Identify the preparation type.
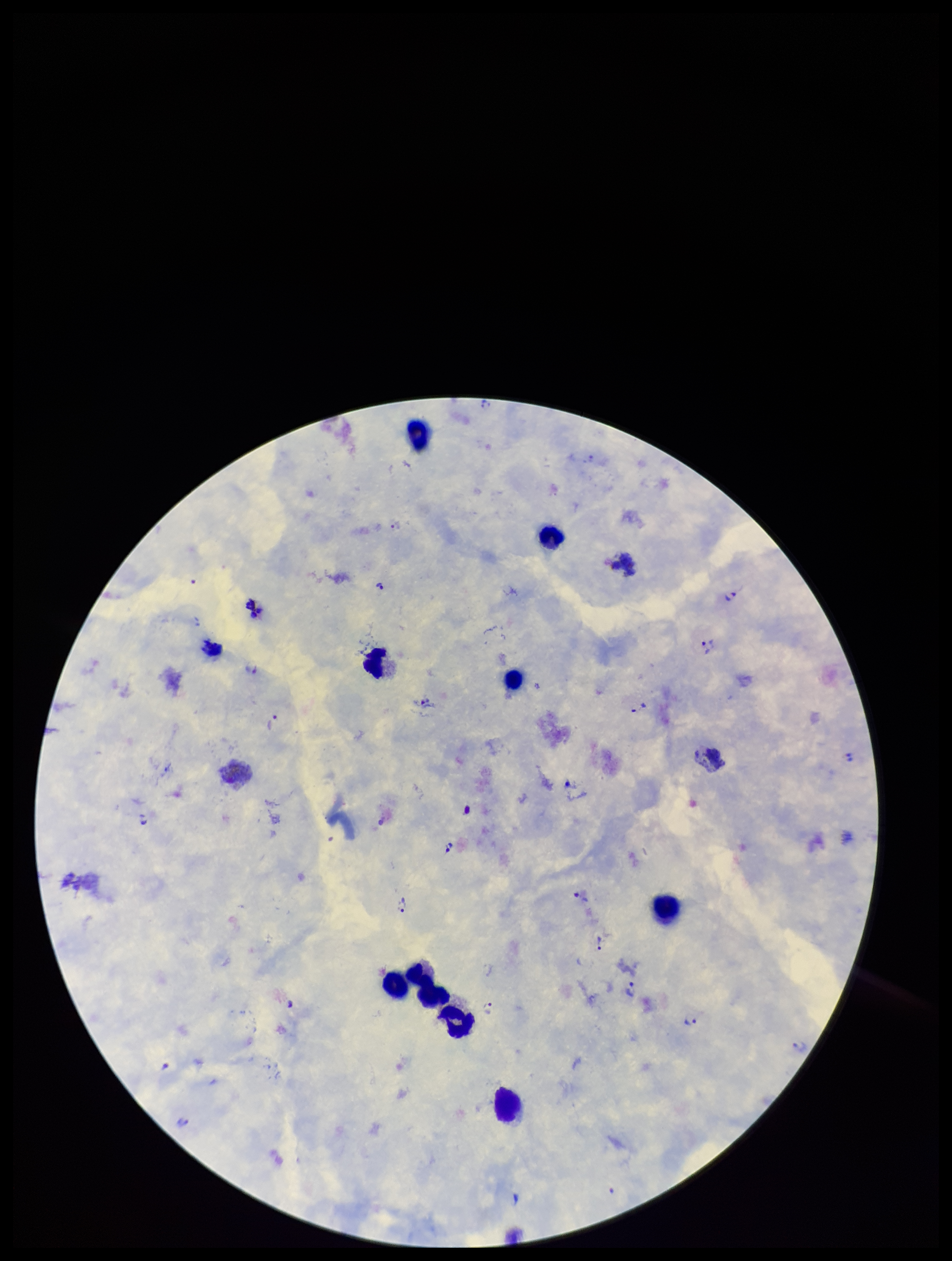

It is a thick blood smear.

parasite count = 16
leukocyte count = 11
species reported for this patient = Plasmodium vivax
patient malaria status = positive
stain = Giemsa
capture = smartphone photograph through the microscope eyepiece
field of view = single
image size = 952×1261 pixels
Plasmodium parasites = seen